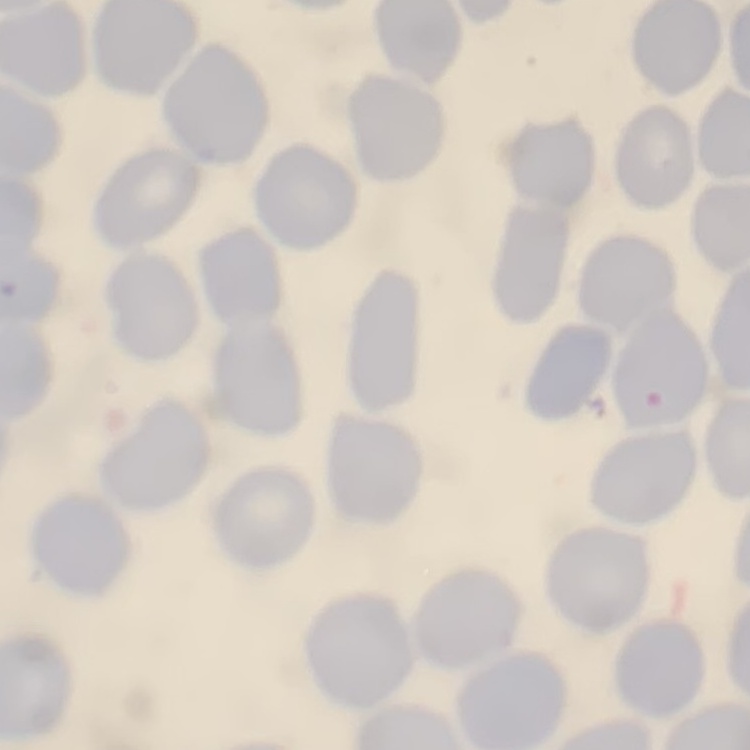
Summary:
  - Red blood cell morphology: no rouleaux formation
  - Image type: one tile cut from a larger photomicrograph
  - Stain: Field's or Giemsa
  - Preparation: thin blood smear